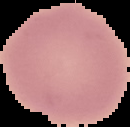
image size = 130×127 pixels
preparation = thin blood film
image type = segmented cell region on a black background
malaria status = uninfected